Outline each blood parasite and name the species.
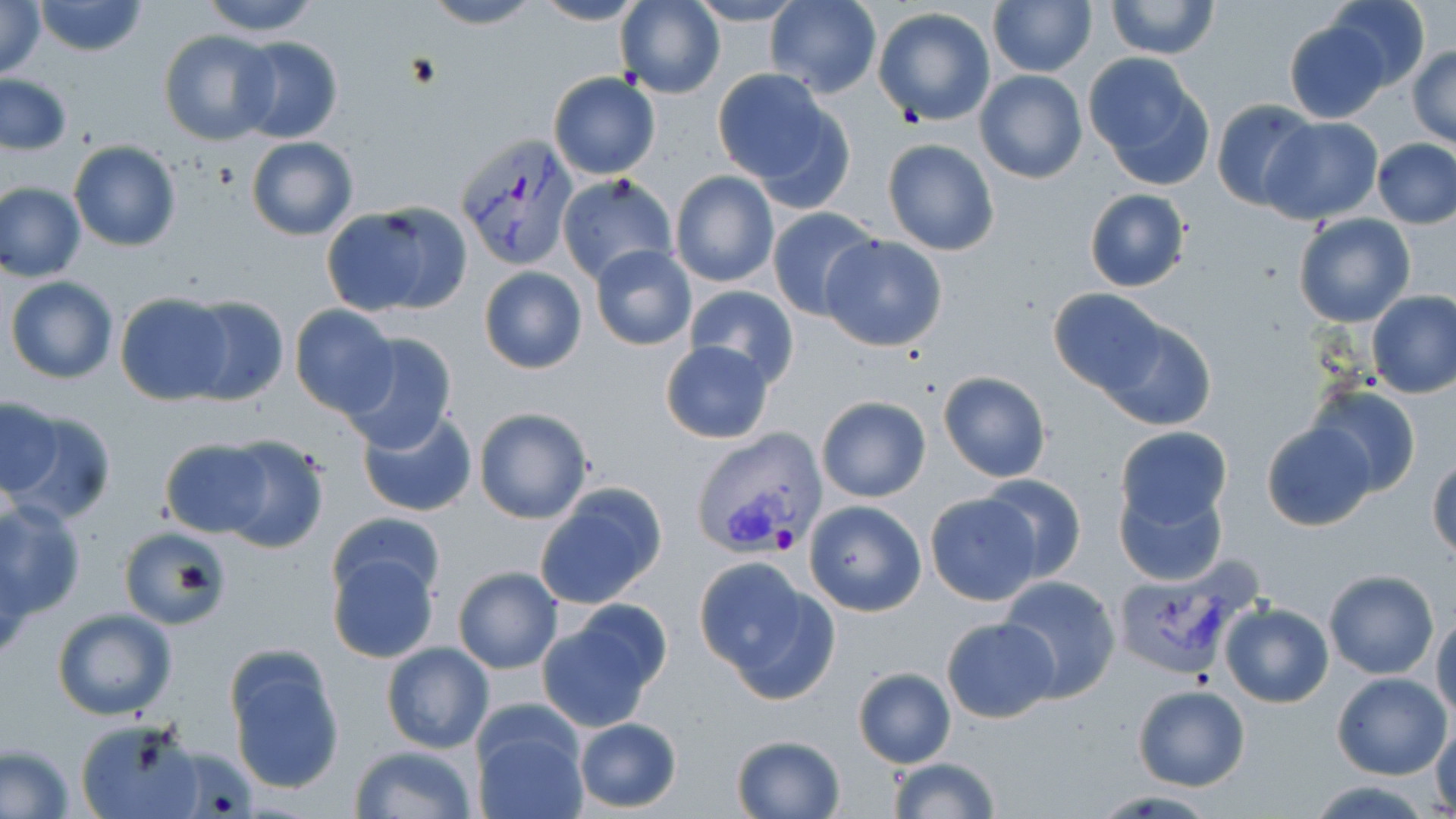
Approximate bounding boxes as (x1, y1, x2, y2) in pixels.
Plasmodium vivax-infected red blood cells: (456, 132, 579, 271), (690, 427, 830, 559), (1120, 557, 1261, 677).
No Plasmodium falciparum, Plasmodium ovale, Plasmodium malariae, Babesia divergens, or Trypanosoma brucei observed.

Uninfected red blood cell locations: (0, 0, 47, 80), (33, 0, 148, 56), (196, 0, 324, 38), (421, 0, 543, 29), (532, 0, 651, 26), (616, 0, 724, 99), (764, 0, 881, 97), (988, 0, 1096, 77), (1105, 0, 1218, 59), (1324, 0, 1432, 91), (687, 1, 803, 27), (872, 7, 998, 127), (1283, 19, 1391, 123), (159, 29, 281, 147), (234, 37, 343, 144), (1409, 46, 1456, 148), (1083, 53, 1214, 189), (974, 69, 1087, 183), (548, 71, 661, 179), (717, 72, 849, 207), (1, 73, 73, 155), (1210, 99, 1318, 211), (1260, 117, 1383, 223), (246, 137, 358, 240), (882, 138, 1000, 256), (69, 139, 181, 251), (1371, 139, 1456, 229), (671, 170, 779, 289), (557, 174, 678, 288), (0, 183, 86, 283), (1083, 188, 1191, 293), (321, 203, 467, 317), (767, 207, 880, 322), (1292, 212, 1415, 328), (820, 236, 947, 351), (590, 246, 696, 350), (479, 267, 585, 375), (5, 276, 118, 384), (684, 285, 799, 387), (1047, 287, 1166, 394), (1367, 290, 1456, 398), (115, 293, 235, 405), (179, 296, 288, 407), (289, 305, 400, 417), (1100, 317, 1218, 431), (338, 332, 459, 452), (659, 342, 774, 444), (938, 371, 1051, 482), (1307, 383, 1421, 498), (1, 395, 63, 500), (815, 395, 931, 501), (5, 406, 114, 524), (473, 406, 594, 525), (357, 407, 478, 520), (1261, 422, 1376, 530), (1114, 426, 1231, 529), (211, 432, 331, 555), (159, 438, 271, 536), (1427, 458, 1456, 559), (980, 475, 1087, 582), (1115, 482, 1226, 586), (533, 483, 670, 611), (924, 493, 1044, 606), (803, 499, 928, 616), (0, 500, 87, 621), (329, 510, 445, 606), (116, 527, 227, 628), (326, 550, 441, 664), (696, 557, 833, 698), (452, 566, 563, 674), (1322, 570, 1439, 679), (997, 574, 1122, 702), (1219, 602, 1334, 709), (537, 604, 670, 731), (52, 607, 179, 721), (1432, 609, 1456, 723), (942, 616, 1060, 724), (381, 641, 494, 753), (222, 645, 345, 796), (851, 667, 957, 767), (1332, 671, 1451, 779), (1134, 684, 1251, 791), (472, 711, 586, 819), (571, 716, 682, 813), (75, 717, 207, 819), (1429, 718, 1456, 815), (730, 734, 844, 818), (0, 744, 77, 817), (350, 745, 477, 819), (887, 756, 1000, 818), (1304, 781, 1438, 818). Slide-level diagnosis: Plasmodium vivax. Optical microscopy. May-Grünwald-Giemsa-stained preparation. Image is 1456×819 pixels. 1000x magnification. One field of a larger specimen. Thin blood film.